Locate and identify every blood parasite.
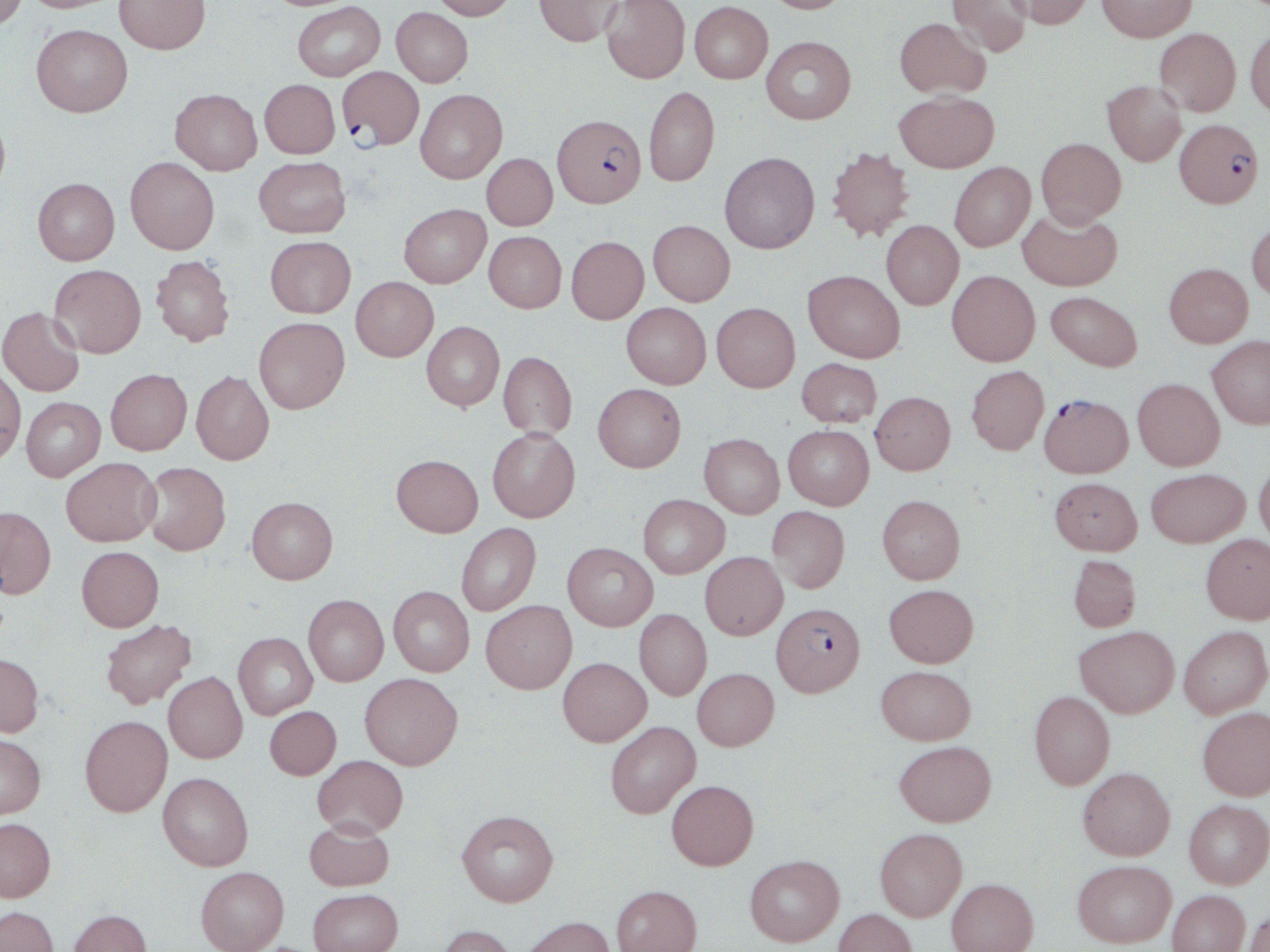

Approximate bounding boxes as [x1, y1, x2, y2] in pixels.
Plasmodium falciparum-infected red blood cells: [336, 66, 424, 150], [552, 114, 646, 208], [1174, 118, 1264, 208], [1040, 393, 1132, 478], [772, 602, 865, 697].
No Plasmodium ovale, Plasmodium malariae, Plasmodium vivax, Babesia divergens, or Trypanosoma brucei observed.

slide_level_diagnosis: Plasmodium falciparum
modality: light microscopy
magnification: 1000x
preparation: thin blood smear
image_size: 1270×952 pixels
stain: May-Grünwald-Giemsa
uninfected_red_blood_cell_locations: 'approximate bounding boxes as [x1, y1, x2, y2] in pixels: [0, 0, 26, 29], [21, 0, 122, 13], [115, 0, 210, 54], [430, 0, 517, 19], [534, 0, 622, 46], [763, 0, 851, 13], [947, 0, 1034, 57], [1006, 0, 1094, 29], [1097, 0, 1197, 42], [601, 1, 691, 84], [293, 2, 385, 81], [689, 2, 772, 83], [391, 7, 473, 86], [894, 17, 990, 98], [31, 23, 133, 116], [1245, 24, 1270, 118], [1154, 27, 1241, 116], [761, 36, 856, 124], [259, 79, 339, 158], [1102, 80, 1186, 166], [644, 86, 719, 186], [170, 89, 262, 175], [415, 89, 507, 183], [895, 91, 999, 173], [0, 108, 10, 201], [1036, 137, 1126, 227], [826, 146, 915, 242], [719, 151, 819, 253], [481, 153, 557, 230], [254, 156, 351, 238], [125, 157, 219, 254], [949, 162, 1035, 251], [33, 177, 120, 265], [399, 204, 491, 287], [1017, 207, 1122, 291], [1247, 219, 1270, 301], [648, 220, 735, 306], [881, 220, 963, 309], [484, 231, 566, 312], [265, 235, 356, 317], [566, 236, 649, 324], [152, 255, 235, 346], [1164, 262, 1253, 347], [49, 264, 146, 358], [803, 270, 905, 363], [947, 270, 1040, 366], [351, 276, 438, 361], [1046, 291, 1142, 371], [622, 302, 711, 388], [712, 303, 800, 392], [0, 307, 85, 397], [254, 317, 349, 413], [421, 321, 504, 410], [1207, 336, 1270, 429], [498, 351, 577, 439], [797, 358, 882, 427], [966, 365, 1049, 455], [0, 366, 26, 465], [106, 369, 192, 455], [191, 371, 274, 465], [1133, 378, 1225, 470], [593, 383, 686, 472], [871, 391, 955, 475], [21, 397, 105, 481], [783, 425, 874, 510], [487, 428, 580, 522], [699, 433, 784, 518], [391, 454, 483, 537], [61, 457, 161, 546], [1254, 460, 1270, 547], [141, 461, 230, 555], [1146, 468, 1250, 546], [1050, 477, 1142, 555], [638, 494, 729, 578], [877, 494, 965, 584], [246, 496, 338, 584], [0, 506, 56, 599], [767, 506, 849, 593], [456, 523, 541, 616], [1200, 532, 1270, 624], [562, 542, 658, 630], [76, 546, 164, 631], [700, 551, 787, 639], [1068, 554, 1141, 632], [884, 584, 978, 667], [388, 586, 475, 676], [303, 595, 388, 685], [481, 600, 577, 694], [634, 609, 712, 700], [100, 619, 196, 709], [1179, 625, 1270, 718], [1075, 626, 1179, 718], [234, 632, 317, 719], [0, 653, 44, 737], [558, 657, 651, 746], [876, 665, 975, 745], [692, 668, 779, 750], [163, 672, 247, 763], [360, 672, 462, 769], [1030, 691, 1115, 790], [265, 706, 341, 779], [1197, 706, 1270, 800], [80, 716, 172, 817], [605, 721, 701, 818], [0, 733, 45, 819], [894, 740, 996, 826], [313, 755, 408, 837], [1078, 767, 1175, 860], [158, 772, 253, 870], [667, 780, 758, 870], [1184, 800, 1269, 888], [457, 809, 559, 907], [0, 818, 55, 902], [304, 818, 394, 891], [875, 828, 967, 921], [745, 855, 844, 946], [1072, 860, 1176, 947], [195, 866, 288, 952], [946, 878, 1038, 952], [612, 885, 702, 952], [308, 888, 403, 952], [1167, 889, 1250, 952], [0, 906, 59, 952], [832, 908, 918, 952], [68, 909, 152, 952], [1242, 909, 1270, 952], [521, 916, 616, 952], [437, 924, 518, 952]'
field_of_view: one of a larger specimen